Locate every blood parasite and identify its species.
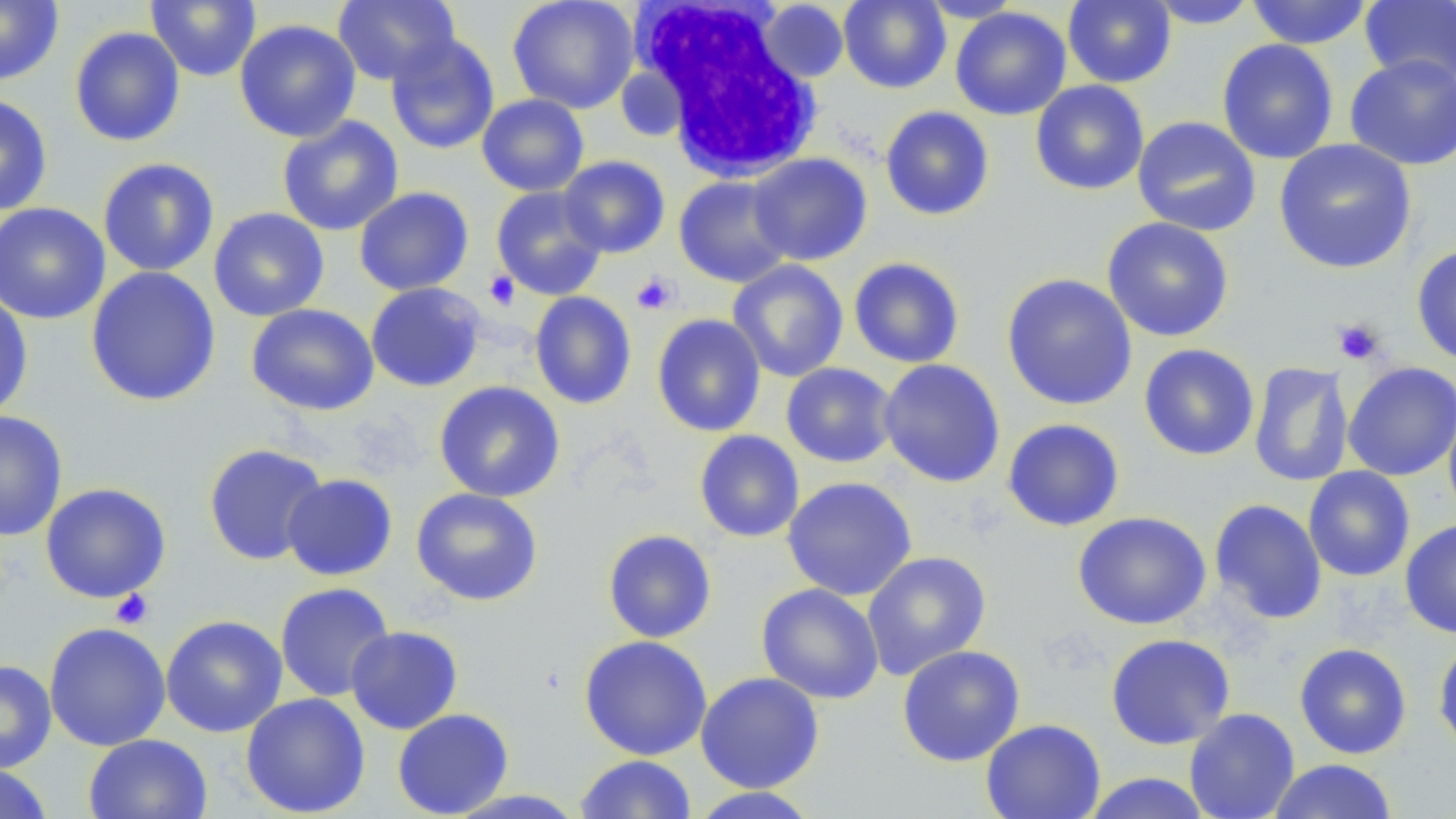

No blood parasites seen.

Approximate bounding boxes as named x1/y1/x2/y2 corners in pixels. Platelet locations: (x1=484, y1=271, x2=521, y2=311), (x1=631, y1=272, x2=680, y2=315), (x1=1332, y1=318, x2=1385, y2=365), (x1=110, y1=588, x2=153, y2=630). White blood cell locations: (x1=635, y1=4, x2=824, y2=182). Uninfected red blood cell locations: (x1=0, y1=0, x2=64, y2=86), (x1=145, y1=0, x2=261, y2=82), (x1=332, y1=0, x2=461, y2=86), (x1=507, y1=0, x2=639, y2=113), (x1=839, y1=0, x2=951, y2=93), (x1=917, y1=0, x2=1025, y2=23), (x1=1063, y1=0, x2=1177, y2=88), (x1=1245, y1=0, x2=1374, y2=49), (x1=758, y1=1, x2=850, y2=83), (x1=1146, y1=1, x2=1260, y2=29), (x1=1359, y1=1, x2=1456, y2=88), (x1=950, y1=6, x2=1071, y2=120), (x1=234, y1=19, x2=361, y2=142), (x1=69, y1=26, x2=186, y2=147), (x1=385, y1=33, x2=500, y2=155), (x1=1216, y1=39, x2=1339, y2=164), (x1=1345, y1=53, x2=1456, y2=170), (x1=1030, y1=80, x2=1149, y2=196), (x1=0, y1=93, x2=53, y2=216), (x1=476, y1=93, x2=590, y2=197), (x1=879, y1=106, x2=995, y2=221), (x1=277, y1=116, x2=404, y2=236), (x1=1132, y1=116, x2=1262, y2=236), (x1=1274, y1=139, x2=1417, y2=274), (x1=748, y1=153, x2=873, y2=266), (x1=557, y1=155, x2=670, y2=258), (x1=97, y1=158, x2=220, y2=277), (x1=673, y1=175, x2=793, y2=287), (x1=490, y1=185, x2=608, y2=300), (x1=354, y1=186, x2=474, y2=296), (x1=0, y1=203, x2=111, y2=325), (x1=208, y1=207, x2=330, y2=321), (x1=1101, y1=217, x2=1235, y2=342), (x1=1411, y1=244, x2=1456, y2=365), (x1=848, y1=257, x2=965, y2=368), (x1=727, y1=260, x2=849, y2=382), (x1=86, y1=266, x2=221, y2=407), (x1=1001, y1=273, x2=1138, y2=411), (x1=365, y1=282, x2=486, y2=392), (x1=0, y1=290, x2=34, y2=422), (x1=529, y1=291, x2=637, y2=410), (x1=246, y1=303, x2=379, y2=416), (x1=651, y1=314, x2=766, y2=437), (x1=1139, y1=343, x2=1259, y2=460), (x1=878, y1=358, x2=1006, y2=487), (x1=1249, y1=361, x2=1354, y2=488), (x1=1343, y1=361, x2=1456, y2=480), (x1=781, y1=362, x2=898, y2=468), (x1=433, y1=380, x2=565, y2=502), (x1=1443, y1=396, x2=1456, y2=527), (x1=0, y1=410, x2=68, y2=541), (x1=1002, y1=418, x2=1125, y2=532), (x1=694, y1=430, x2=805, y2=543), (x1=203, y1=443, x2=329, y2=566), (x1=1303, y1=466, x2=1415, y2=582), (x1=281, y1=473, x2=398, y2=581), (x1=781, y1=476, x2=918, y2=601), (x1=40, y1=482, x2=171, y2=603), (x1=410, y1=487, x2=544, y2=606), (x1=1209, y1=499, x2=1327, y2=625), (x1=1073, y1=511, x2=1211, y2=630), (x1=1400, y1=518, x2=1456, y2=639), (x1=602, y1=529, x2=717, y2=644), (x1=862, y1=550, x2=992, y2=680), (x1=275, y1=582, x2=395, y2=702), (x1=756, y1=583, x2=885, y2=704), (x1=160, y1=615, x2=288, y2=737), (x1=43, y1=622, x2=171, y2=751), (x1=345, y1=625, x2=463, y2=734), (x1=1105, y1=633, x2=1235, y2=750), (x1=578, y1=635, x2=713, y2=760), (x1=1433, y1=637, x2=1456, y2=756), (x1=1294, y1=642, x2=1412, y2=759), (x1=897, y1=645, x2=1025, y2=766), (x1=0, y1=660, x2=57, y2=774), (x1=695, y1=671, x2=824, y2=793), (x1=240, y1=692, x2=371, y2=818), (x1=392, y1=708, x2=514, y2=818), (x1=1184, y1=708, x2=1300, y2=819), (x1=980, y1=718, x2=1106, y2=819), (x1=83, y1=733, x2=212, y2=819), (x1=575, y1=754, x2=697, y2=818), (x1=1267, y1=759, x2=1398, y2=818), (x1=0, y1=764, x2=53, y2=819), (x1=1079, y1=772, x2=1215, y2=819), (x1=686, y1=787, x2=823, y2=818), (x1=444, y1=788, x2=588, y2=818). Slide-level diagnosis: no evidence of blood parasites. Thin blood film. 1000x magnification. Single field of view. May-Grünwald-Giemsa stain. Image is 1456×819 pixels. Light microscopy.